Locate and identify every blood parasite.
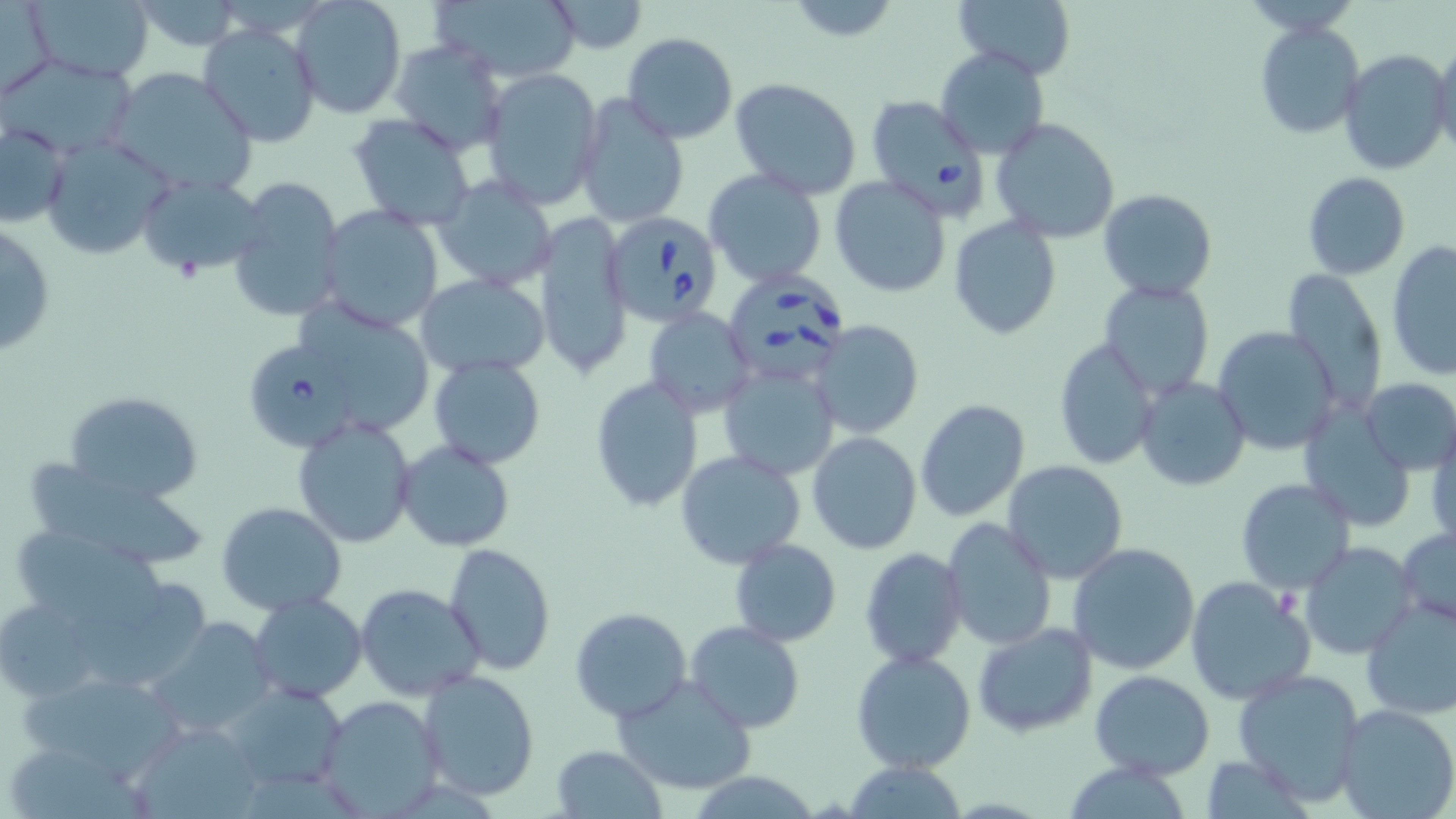
Approximate bounding boxes as [x1, y1, x2, y2] in pixels.
Babesia divergens-infected red blood cells: [864, 94, 990, 218], [606, 214, 726, 327], [725, 272, 847, 385], [234, 328, 386, 451].
No Plasmodium falciparum, Plasmodium ovale, Plasmodium malariae, Plasmodium vivax, or Trypanosoma brucei observed.

Uninfected red blood cell locations: [23, 0, 158, 84], [129, 0, 251, 52], [290, 0, 406, 120], [430, 0, 584, 85], [543, 0, 650, 54], [952, 0, 1077, 80], [2, 2, 57, 99], [783, 2, 904, 46], [198, 20, 324, 149], [1254, 22, 1364, 140], [622, 32, 738, 143], [1430, 37, 1456, 158], [390, 39, 509, 157], [935, 46, 1051, 160], [1338, 49, 1449, 174], [107, 66, 257, 197], [476, 67, 604, 210], [729, 78, 862, 202], [574, 94, 689, 228], [349, 113, 477, 229], [991, 117, 1121, 243], [1, 120, 71, 230], [41, 134, 173, 260], [703, 168, 828, 288], [135, 172, 267, 279], [1302, 172, 1410, 279], [224, 174, 346, 326], [830, 175, 953, 297], [431, 176, 555, 293], [1098, 188, 1217, 301], [317, 206, 446, 334], [533, 210, 633, 379], [949, 217, 1060, 340], [1, 219, 56, 359], [1386, 239, 1455, 380], [415, 272, 551, 379], [1283, 272, 1389, 415], [1098, 280, 1215, 399], [1117, 292, 1234, 479], [284, 298, 435, 439], [644, 306, 755, 415], [810, 320, 924, 439], [1211, 326, 1341, 455], [1054, 337, 1160, 470], [428, 355, 547, 469], [718, 360, 840, 482], [590, 376, 704, 513], [1135, 377, 1251, 491], [1358, 378, 1456, 474], [64, 390, 204, 504], [917, 399, 1033, 521], [1300, 406, 1415, 530], [1427, 412, 1456, 552], [292, 415, 418, 548], [807, 432, 922, 553], [395, 438, 519, 553], [676, 451, 805, 569], [1002, 460, 1130, 584], [26, 463, 207, 569], [1235, 478, 1356, 595], [216, 502, 348, 617], [941, 518, 1057, 652], [5, 521, 172, 639], [1396, 527, 1456, 629], [729, 537, 842, 647], [443, 542, 556, 673], [1068, 542, 1200, 674], [1300, 542, 1418, 660], [422, 545, 550, 783], [861, 546, 967, 670], [1185, 576, 1314, 705], [354, 582, 481, 703], [250, 593, 368, 704], [0, 596, 108, 699], [1359, 597, 1456, 720], [570, 607, 692, 724], [142, 617, 278, 740], [685, 621, 809, 735], [973, 622, 1099, 738], [850, 649, 978, 775], [14, 668, 190, 782], [418, 669, 540, 801], [1231, 669, 1368, 804], [1090, 670, 1214, 778], [610, 676, 758, 794], [223, 680, 350, 792], [317, 693, 446, 816], [1335, 704, 1456, 819], [128, 718, 263, 819], [551, 743, 666, 817], [840, 760, 973, 817]. Slide-level diagnosis: Babesia divergens. Captured at 1000x magnification. Image is 1456×819 pixels. May-Grünwald-Giemsa-stained preparation. Light microscopy. Thin blood smear. One field of a larger specimen.